State the preparation type.
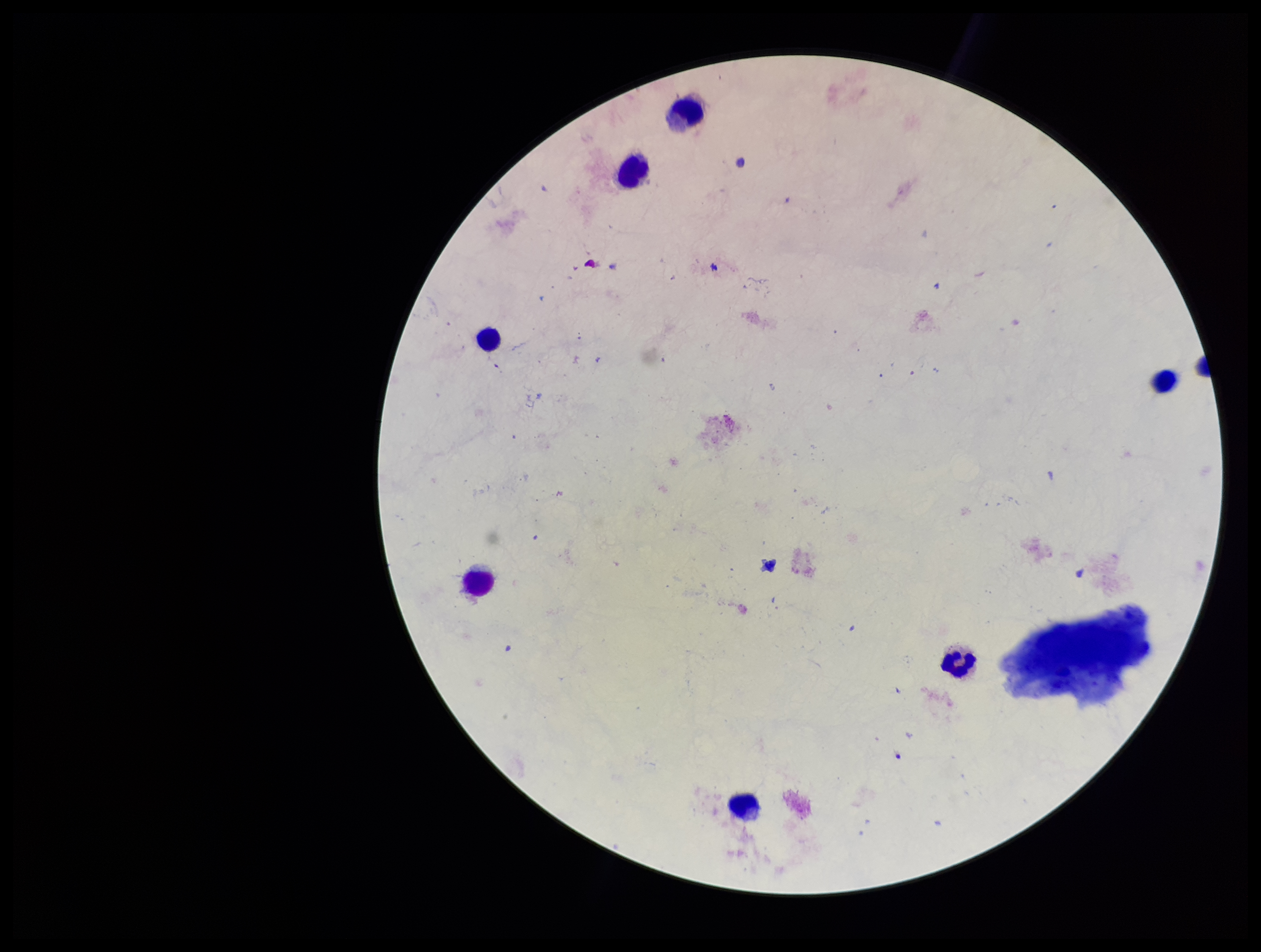
Thick.

Parasite count: 0. Plasmodium parasites: none seen. Photographed through the microscope eyepiece with a smartphone camera. Giemsa stain. Patient malaria status: negative. Leukocyte count: 8. Single field of view. Image is 1261×952 pixels.